Report the malaria status of this cell.
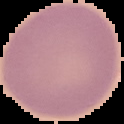

It is uninfected.

image_size: 124×124 pixels
preparation: thin blood film
image_type: cell region segmented out of the field of view; surrounding area masked to black